Give the position of every malaria parasite.
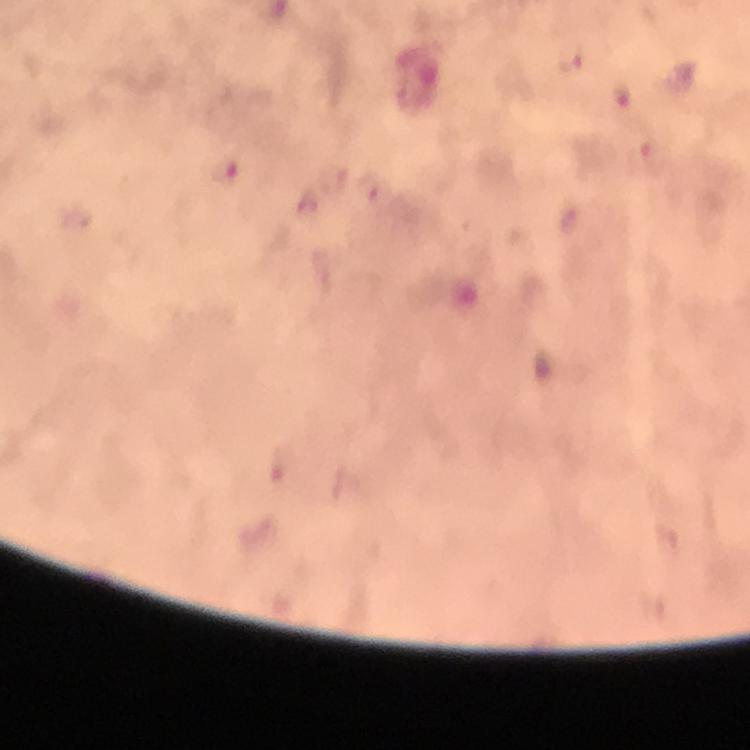

Approximate object centers, in pixels from the top-left corner.
Malaria parasites: (x=569, y=59), (x=623, y=95), (x=224, y=171).

stain = Giemsa
capture = smartphone photograph through a microscope
cropped from = one field of view
context = from a diagnostic examination for malaria
image size = 750×750 pixels
preparation = thick blood film
magnification = 100x
immersion oil = applied